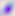
identification: Toxoplasma gondii
magnification: 400x
modality: photomicrograph